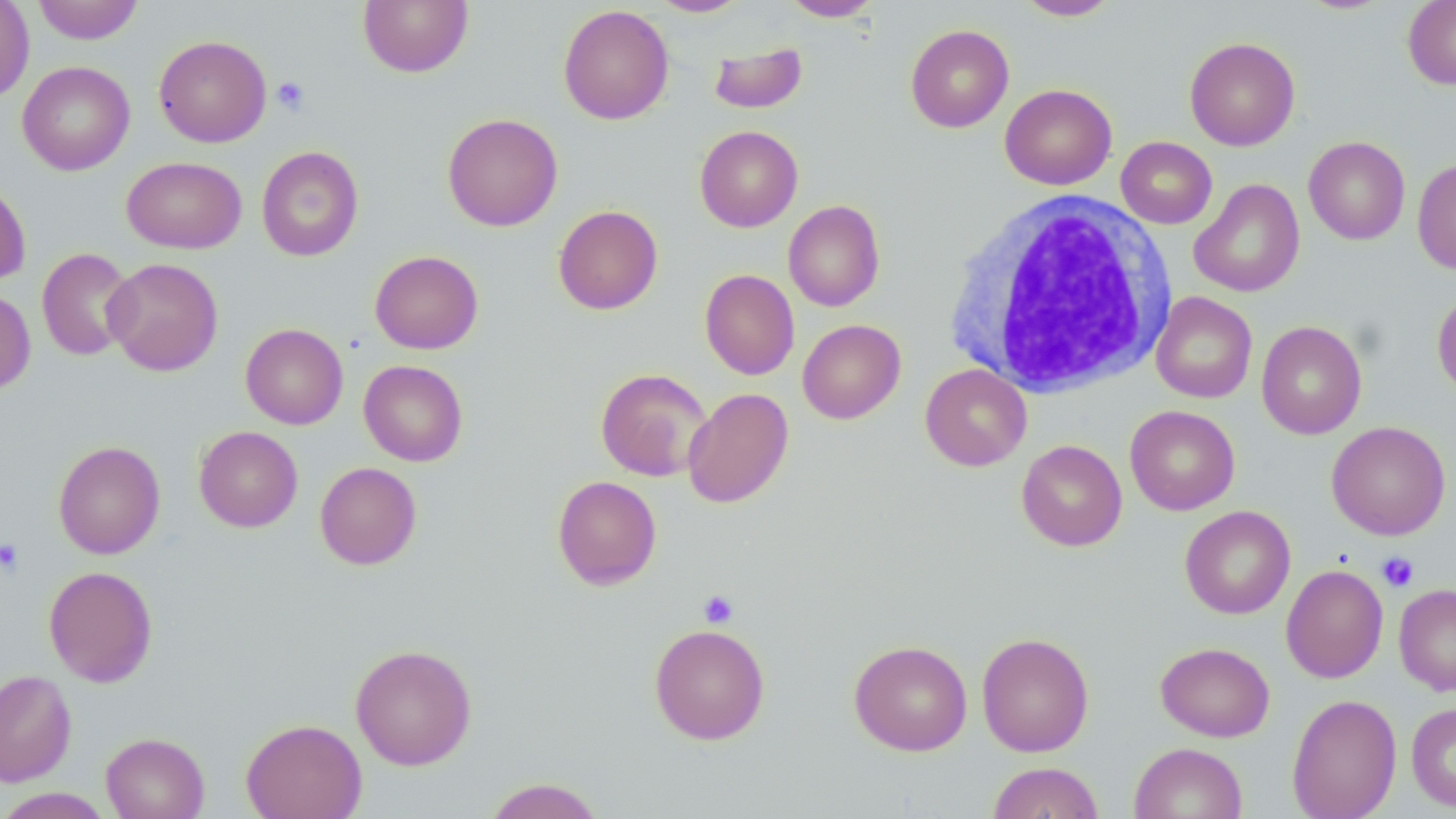

slide-level diagnosis = no evidence of blood parasites
field of view = single
preparation = thin blood film
magnification = 1000x
image size = 1456×819 pixels
platelet locations = approximate bounding boxes as (x1,y1)-(x2,y2) corner pairs in pixels: (271,77)-(310,114), (0,538)-(23,576), (1376,551)-(1419,593), (698,590)-(739,628)
stain = May-Grünwald-Giemsa
uninfected red blood cell locations = approximate bounding boxes as (x1,y1)-(x2,y2) corner pairs in pixels: (0,0)-(35,104), (32,0)-(144,44), (357,0)-(473,77), (649,0)-(751,17), (781,0)-(882,21), (1015,0)-(1120,21), (1403,1)-(1456,89), (558,4)-(674,125), (905,24)-(1014,132), (154,35)-(272,147), (1184,36)-(1300,150), (709,41)-(807,114), (17,61)-(135,175), (1000,83)-(1117,190), (442,113)-(563,232), (694,125)-(803,232), (1116,136)-(1217,229), (1303,136)-(1410,245), (256,146)-(364,262), (122,156)-(246,254), (1412,157)-(1456,275), (0,178)-(31,285), (1189,178)-(1305,297), (783,200)-(885,312), (553,205)-(663,315), (37,248)-(136,361), (370,250)-(483,354), (103,257)-(223,376), (700,269)-(800,380), (0,287)-(36,395), (1432,287)-(1456,400), (1151,292)-(1257,403), (797,319)-(906,423), (1256,320)-(1367,439), (240,323)-(348,430), (358,360)-(468,466), (920,364)-(1032,471), (595,368)-(712,482), (682,387)-(794,508), (1125,405)-(1240,515), (1327,421)-(1451,540), (194,426)-(303,532), (1016,439)-(1127,551), (53,440)-(165,559), (315,462)-(422,570), (552,475)-(662,590), (1179,505)-(1295,619), (1281,564)-(1388,683), (43,565)-(158,687), (1394,583)-(1456,695), (649,623)-(770,744), (976,632)-(1094,756), (848,639)-(973,756), (1155,642)-(1275,741), (350,644)-(476,770), (0,668)-(77,787), (1287,694)-(1402,819), (1406,701)-(1456,812), (241,718)-(367,819), (101,731)-(210,819), (1129,742)-(1248,819), (987,761)-(1104,819), (483,777)-(606,819), (0,788)-(114,818)
modality = optical microscopy
white blood cell locations = approximate bounding boxes as (x1,y1)-(x2,y2) corner pairs in pixels: (946,191)-(1175,396)